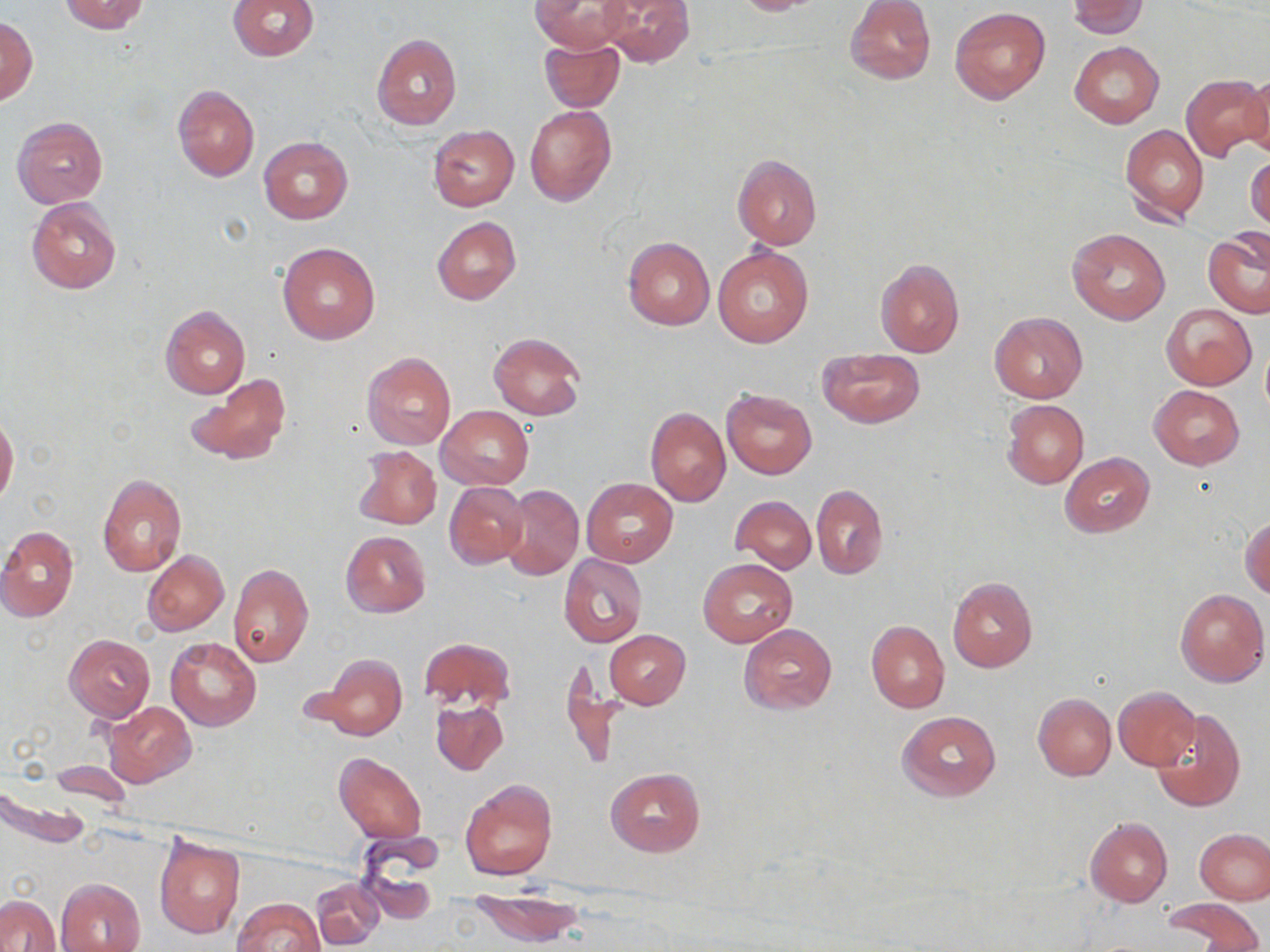
slide-level diagnosis = no evidence of blood parasites
preparation = thin blood smear
magnification = 1000x
modality = light microscopy
uninfected red blood cell locations = approximate bounding boxes as (x1, y1, x2, y2) in pixels: (57, 0, 150, 34), (227, 0, 317, 60), (600, 0, 696, 66), (727, 0, 824, 15), (846, 0, 936, 84), (531, 1, 631, 54), (1066, 1, 1149, 38), (950, 7, 1050, 104), (0, 17, 37, 106), (372, 34, 461, 130), (538, 37, 625, 113), (1069, 41, 1164, 128), (1244, 72, 1270, 162), (1181, 73, 1269, 161), (172, 84, 260, 181), (525, 106, 616, 207), (11, 115, 109, 208), (426, 124, 521, 212), (1121, 125, 1209, 225), (258, 137, 352, 224), (1247, 152, 1269, 233), (731, 155, 823, 249), (26, 197, 122, 294), (433, 216, 521, 305), (1067, 227, 1170, 324), (1203, 233, 1270, 319), (623, 237, 714, 330), (278, 241, 379, 344), (712, 245, 814, 348), (875, 258, 964, 358), (1162, 303, 1256, 389), (161, 306, 250, 398), (990, 311, 1087, 403), (488, 332, 586, 421), (1261, 344, 1270, 419), (820, 348, 922, 427), (362, 352, 456, 449), (186, 372, 289, 466), (1149, 386, 1244, 469), (721, 388, 817, 479), (1003, 399, 1088, 489), (437, 406, 533, 490), (645, 406, 730, 506), (0, 415, 19, 506), (352, 445, 442, 530), (1061, 452, 1154, 537), (98, 474, 187, 576), (583, 478, 678, 566), (444, 482, 529, 568), (502, 484, 583, 580), (811, 484, 887, 580), (729, 495, 816, 572), (1241, 516, 1269, 599), (0, 525, 79, 621), (340, 530, 431, 619), (142, 550, 228, 635), (559, 553, 647, 646), (697, 559, 796, 646), (228, 563, 314, 667), (947, 576, 1037, 672), (1176, 589, 1268, 686), (867, 620, 950, 712), (739, 625, 837, 714), (604, 630, 690, 709), (63, 634, 155, 722), (165, 637, 261, 731), (418, 637, 516, 713), (313, 654, 408, 741), (559, 660, 625, 771), (1113, 686, 1200, 770), (1034, 693, 1116, 781), (430, 698, 509, 775), (104, 700, 196, 787), (1151, 709, 1246, 812), (897, 710, 1000, 802), (334, 753, 426, 843), (605, 768, 704, 856), (460, 779, 557, 881), (1085, 816, 1173, 907), (1195, 829, 1270, 903), (153, 832, 245, 939), (356, 838, 441, 925), (56, 878, 146, 952), (312, 879, 383, 949), (472, 890, 585, 947), (1, 895, 57, 952), (233, 898, 325, 952), (1164, 898, 1262, 950)
field of view = one of a larger specimen
image size = 1270×952 pixels
stain = May-Grünwald-Giemsa